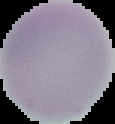
Summary:
  - Preparation: thin blood smear
  - Result: negative for Plasmodium parasites
  - Image type: segmented cell region with the area outside set to black
  - Image size: 115×124 pixels